Assess this cell for malaria.
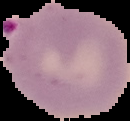
It is parasitized.

Segmented cell region on a black background. From a thin blood film. Image is 130×121 pixels.